Point out each leukocyte.
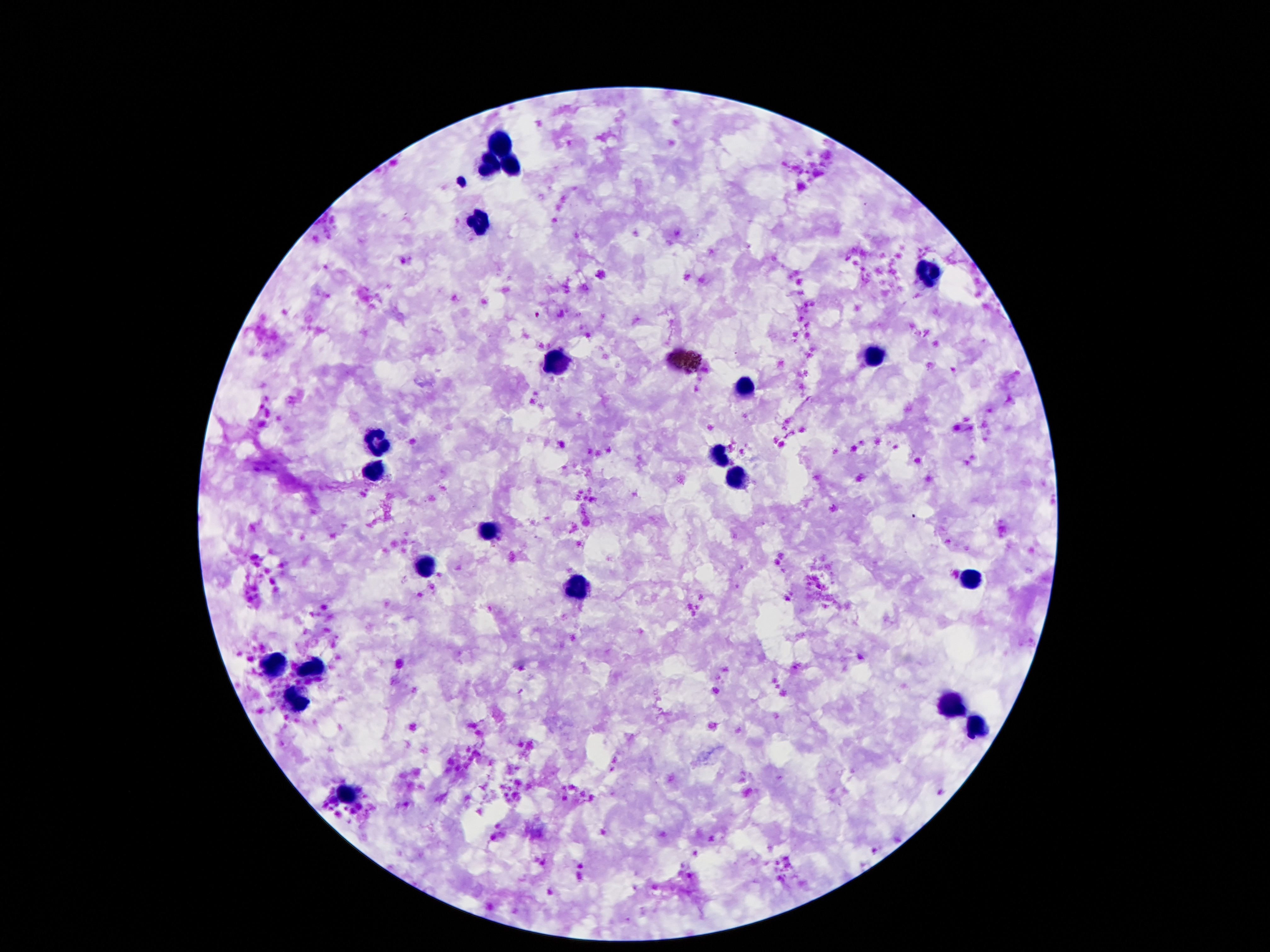
Approximate centers as [x, y] in pixels.
Leukocytes: [501, 141], [486, 161], [513, 163], [476, 221], [931, 272], [872, 357], [555, 365], [743, 385], [377, 440], [718, 459], [372, 469], [733, 478], [489, 533], [424, 566], [578, 587], [271, 665], [308, 665], [293, 702], [948, 704], [976, 730], [345, 796].

capture = smartphone camera through the microscope eyepiece
preparation = thick blood smear
patient malaria status = not infected
image size = 1270×952 pixels
field of view = one from this slide
magnification = 100x
stain = Giemsa